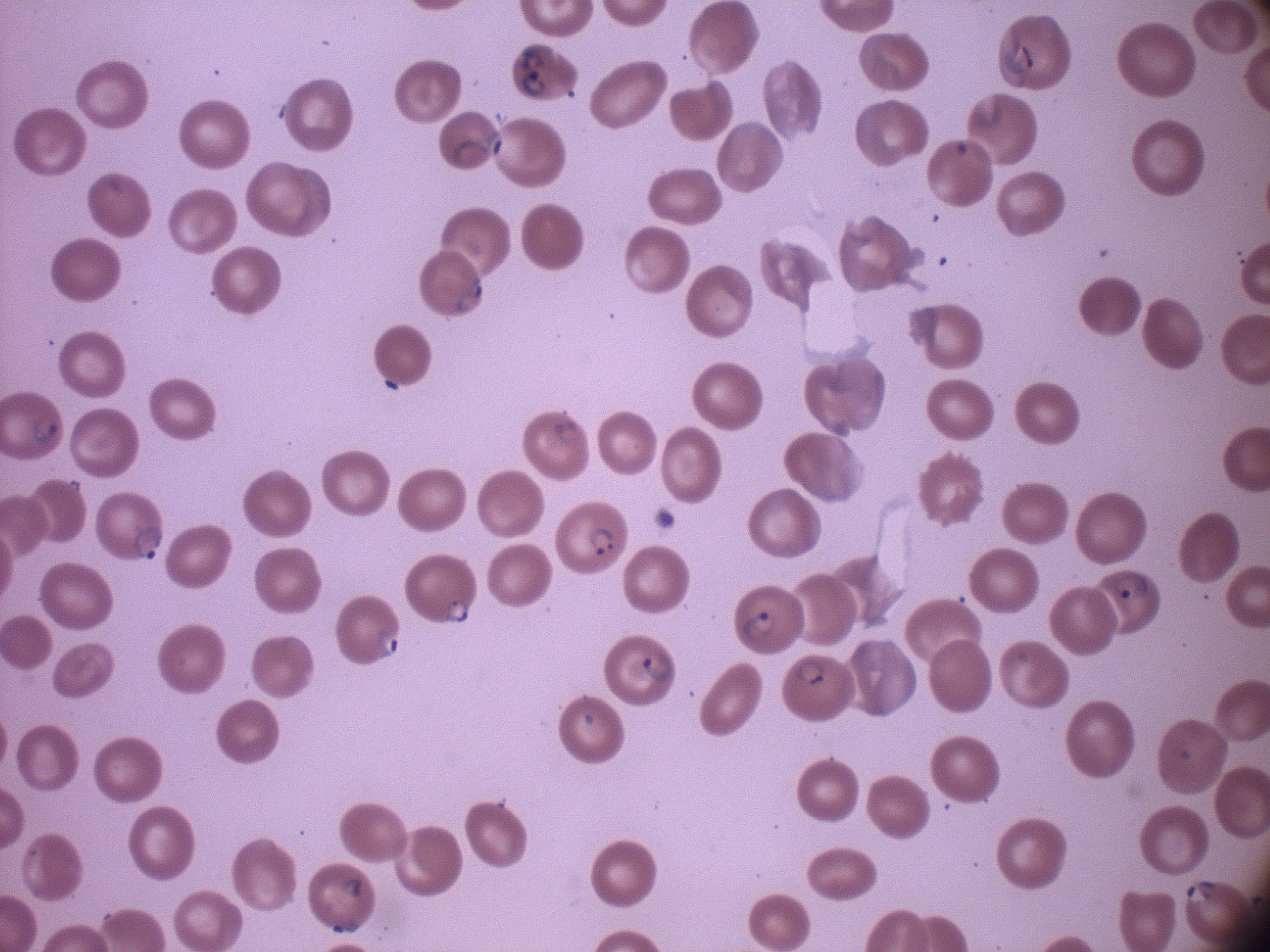
Approximate bounding boxes as (x1, y1, x2, y2) in pixels, from the source annotation, which is not necessarily exhaustive. Ring form locations: (993, 35, 1039, 93), (515, 42, 555, 74), (518, 72, 549, 100), (451, 130, 506, 172), (452, 273, 485, 318), (552, 406, 591, 455), (24, 408, 62, 452), (123, 520, 166, 563), (584, 524, 616, 557), (1105, 566, 1154, 605), (440, 594, 475, 631), (736, 606, 780, 646), (369, 618, 404, 666), (636, 646, 676, 690), (790, 652, 836, 690), (331, 870, 366, 902), (1181, 875, 1220, 907), (327, 910, 366, 938). Leica DM2000 optical microscope with a built-in camera. Species: Plasmodium falciparum. One field from this slide. Giemsa stain. Thin blood smear. Image is 1270×952 pixels. 100x magnification.